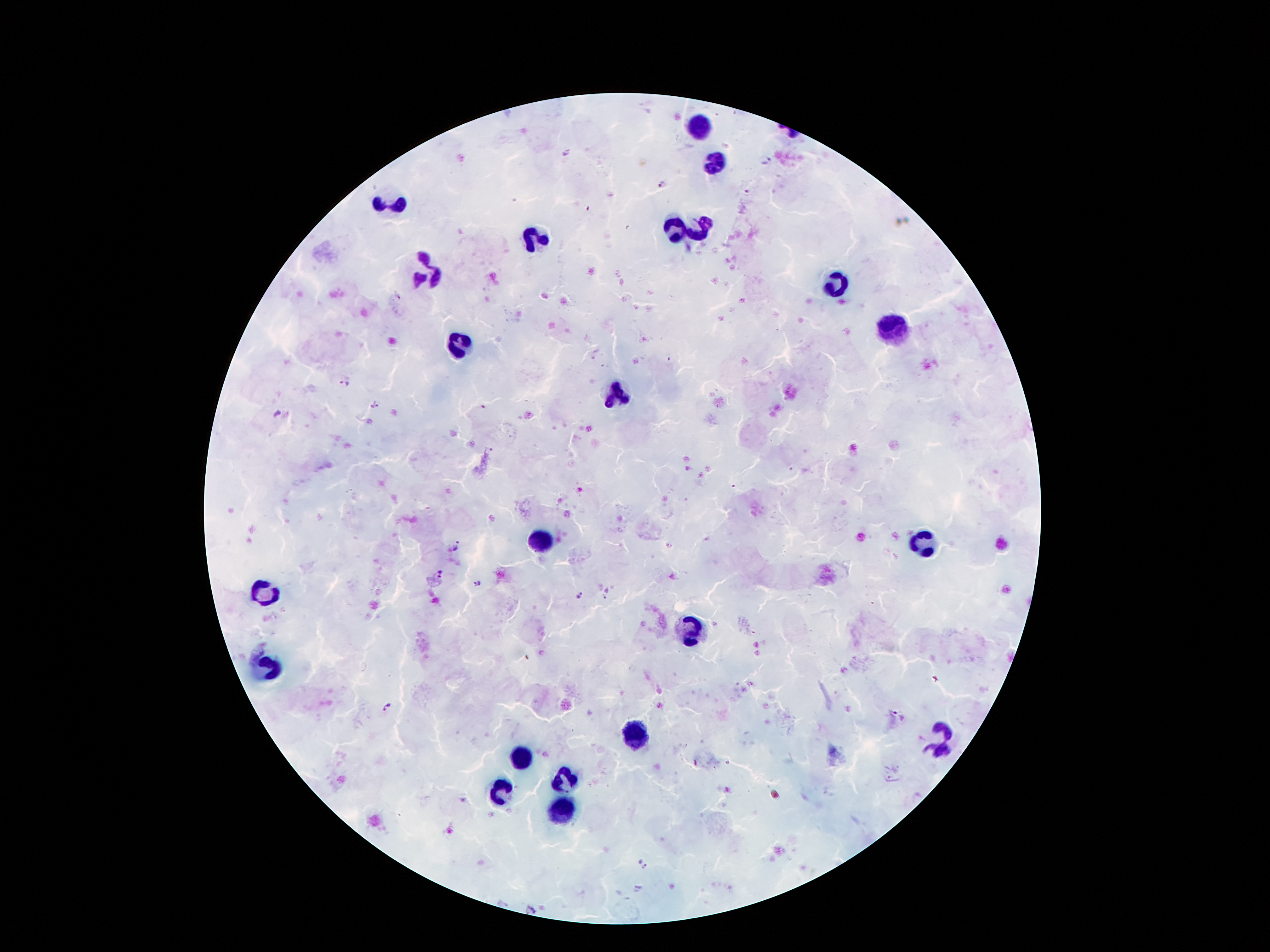

patient_malaria_status: infected with Plasmodium falciparum
image_size: 1270×952 pixels
leukocyte_locations: 'approximate centers as {x, y} in pixels: {699, 127}, {714, 164}, {394, 209}, {674, 227}, {698, 227}, {537, 238}, {428, 273}, {835, 282}, {891, 331}, {462, 341}, {615, 395}, {540, 540}, {923, 543}, {266, 591}, {691, 629}, {266, 666}, {634, 732}, {940, 740}, {521, 757}, {566, 779}, {502, 791}, {562, 809}'
stain: Giemsa
preparation: thick blood film
field_of_view: single
magnification: 100x
capture: smartphone through the microscope eyepiece
plasmodium_parasite_locations: 'approximate centers as {x, y} in pixels: {566, 153}, {766, 162}, {662, 184}, {396, 296}, {344, 384}, {375, 404}, {480, 407}, {489, 449}, {459, 546}, {441, 573}, {476, 582}, {607, 594}, {578, 595}, {389, 707}, {899, 714}, {642, 864}'